State the blood parasite species.
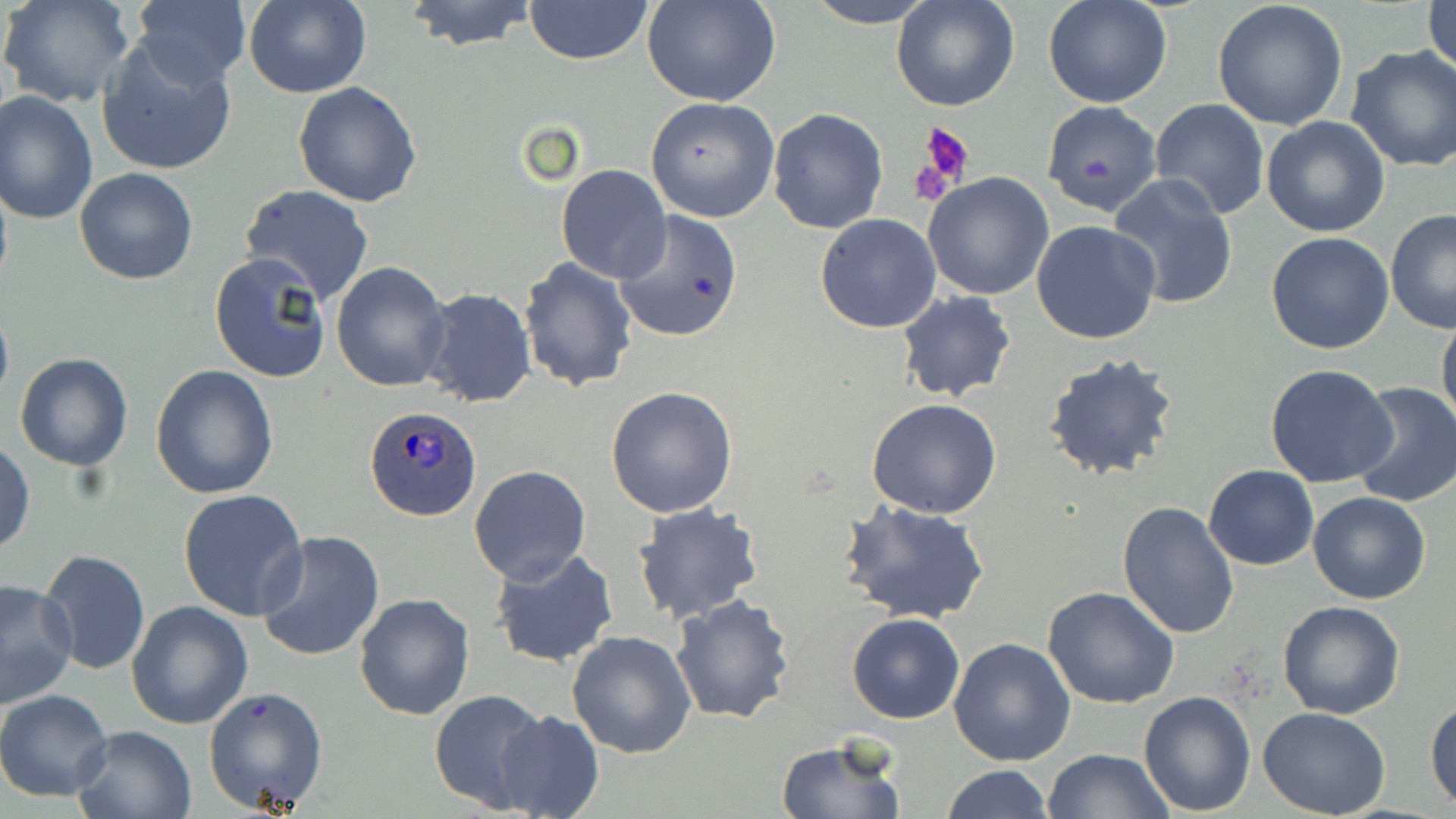
Plasmodium ovale.

Approximate bounding boxes as (x1,y1)-(x2,y2) corner pairs in pixels. Uninfected red blood cell locations: (0,0)-(137,109), (400,0)-(540,50), (644,0)-(782,106), (804,0)-(937,27), (891,0)-(1020,113), (1043,0)-(1171,108), (1425,0)-(1455,84), (132,1)-(252,87), (243,1)-(371,98), (522,1)-(655,65), (1210,1)-(1351,134), (96,37)-(239,176), (1344,46)-(1456,173), (293,82)-(423,207), (0,92)-(99,226), (645,96)-(780,222), (1150,98)-(1270,219), (1040,99)-(1163,216), (768,107)-(889,233), (1261,116)-(1390,238), (555,164)-(671,284), (74,166)-(198,286), (924,173)-(1057,300), (1107,174)-(1239,308), (239,184)-(375,305), (612,211)-(745,344), (1386,211)-(1456,335), (815,214)-(942,333), (1032,221)-(1162,346), (1266,230)-(1395,355), (209,254)-(332,383), (518,258)-(636,392), (330,261)-(451,392), (421,288)-(536,409), (895,290)-(1017,404), (0,300)-(13,411), (1437,312)-(1456,434), (14,352)-(133,471), (1042,352)-(1180,483), (1265,363)-(1397,488), (150,365)-(279,500), (1347,381)-(1456,508), (606,385)-(739,518), (867,400)-(1003,519), (0,440)-(35,555), (469,465)-(591,585), (1204,465)-(1318,570), (178,490)-(310,622), (1308,492)-(1432,604), (841,500)-(992,626), (1118,500)-(1240,639), (632,501)-(767,626), (255,532)-(384,662), (490,547)-(619,667), (38,549)-(150,674), (0,579)-(77,706), (1042,585)-(1181,709), (354,592)-(475,721), (670,593)-(798,724), (1277,599)-(1404,719), (126,601)-(254,730), (847,614)-(965,723), (566,631)-(696,757), (948,638)-(1076,766), (203,686)-(330,815), (428,688)-(549,813), (0,689)-(116,802), (1138,690)-(1256,813), (1425,696)-(1456,812), (1258,707)-(1390,819), (494,710)-(604,819), (72,724)-(197,819), (775,736)-(906,819), (1045,749)-(1172,818), (941,764)-(1053,819). Plasmodium ovale-infected red blood cell locations: (364,407)-(482,521). Platelet locations: (917,123)-(977,190), (910,154)-(957,205). Optical microscopy. Image is 1456×819 pixels. Thin blood smear. May-Grünwald-Giemsa stain. 1000x magnification. Single field of view.